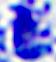

Photomicrograph. A white blood cell is shown. Captured at 400x magnification.